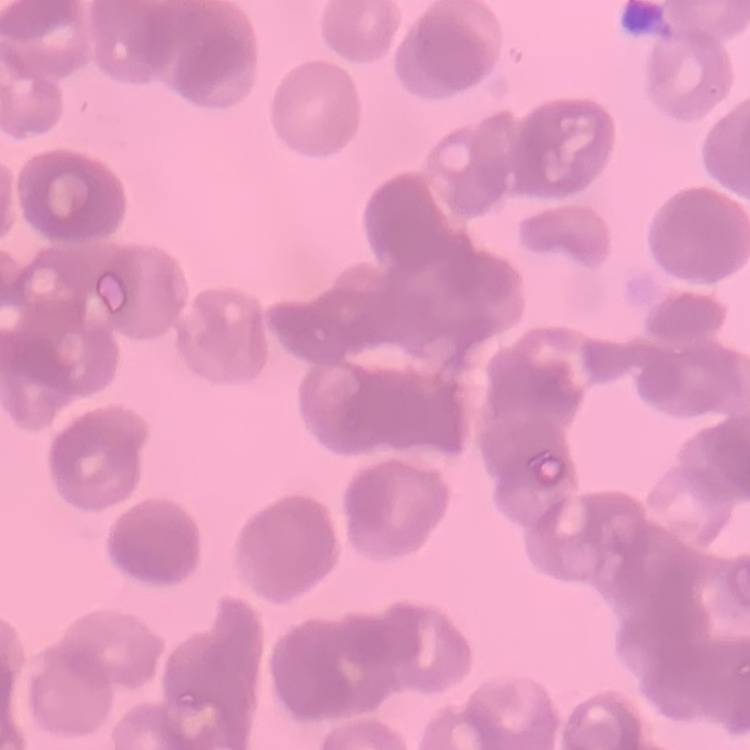

red_blood_cell_morphology: rouleaux formation
stain: Field's or Giemsa
preparation: thin blood film
image_type: one tile cut from a larger photomicrograph